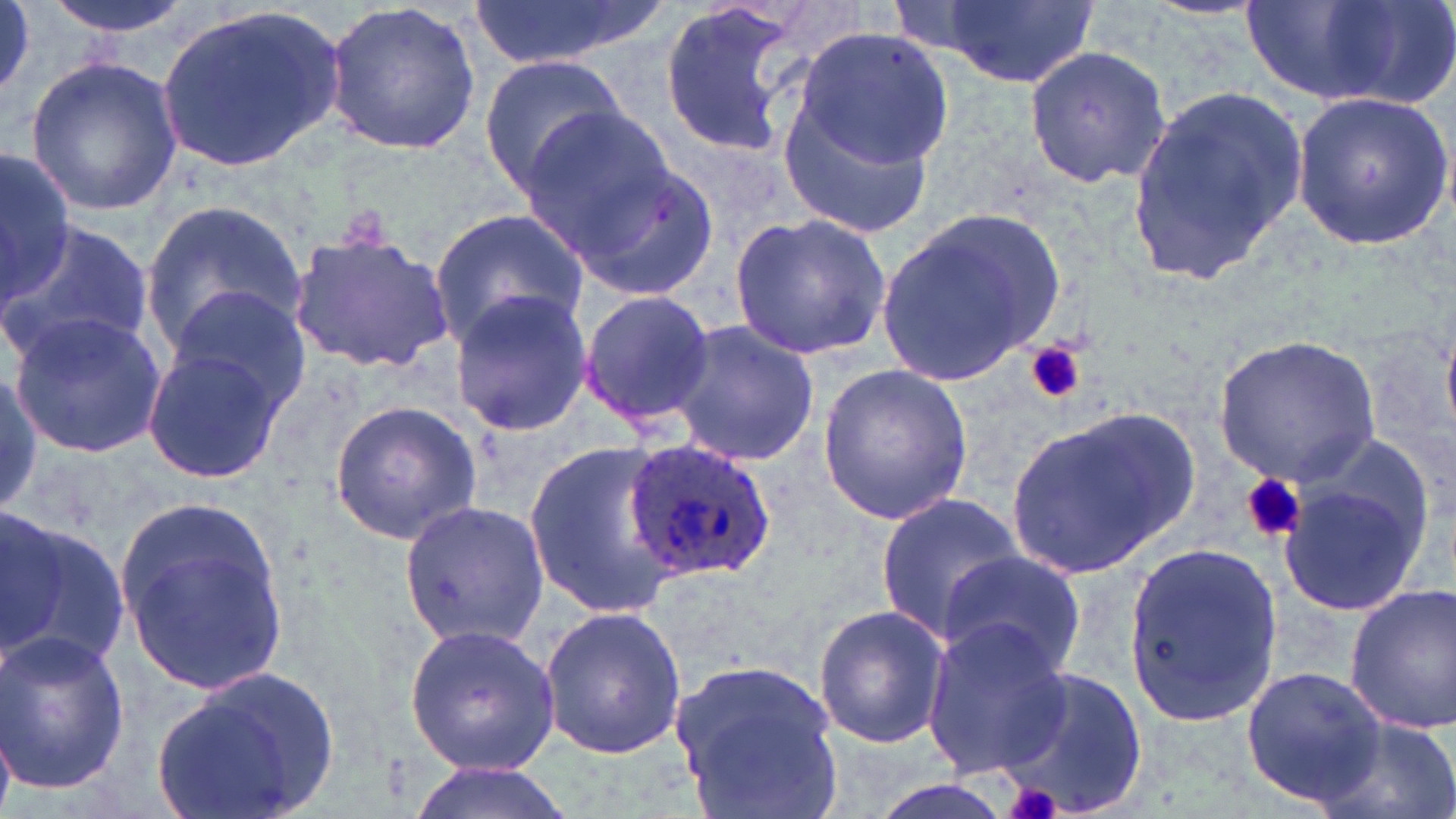

{
  "slide_level_diagnosis": "Plasmodium ovale",
  "modality": "optical microscopy",
  "uninfected_red_blood_cell_locations": "approximate bounding boxes as (x1,y1)-(x2,y2) corner pairs in pixels: (44,0)-(195,42), (472,0)-(669,69), (655,0)-(804,157), (915,0)-(1102,89), (0,1)-(34,96), (325,1)-(483,155), (1235,3)-(1435,110), (152,4)-(347,174), (792,25)-(954,173), (1024,44)-(1172,190), (24,56)-(184,216), (479,57)-(631,200), (1127,83)-(1310,283), (780,86)-(939,240), (1290,93)-(1455,248), (518,105)-(678,261), (0,146)-(75,303), (559,152)-(719,302), (141,198)-(307,354), (876,204)-(1068,388), (429,206)-(590,349), (729,213)-(891,361), (0,219)-(154,367), (288,226)-(454,373), (163,283)-(311,419), (445,286)-(590,437), (577,288)-(716,433), (7,313)-(166,457), (667,318)-(819,468), (1213,334)-(1383,484), (140,347)-(284,487), (816,363)-(976,526), (0,371)-(43,513), (328,400)-(482,544), (1006,402)-(1202,578), (522,438)-(684,619), (1274,458)-(1430,622), (874,490)-(1025,641), (397,499)-(549,651), (115,501)-(290,697), (6,511)-(133,679), (1122,541)-(1282,730), (941,549)-(1086,681), (1342,583)-(1456,734), (540,605)-(688,760), (813,605)-(951,748), (921,619)-(1072,776), (402,622)-(562,778), (0,628)-(132,798), (667,655)-(846,819), (148,664)-(343,819), (1241,664)-(1391,808), (991,667)-(1150,819), (1313,714)-(1456,819), (401,760)-(581,819), (865,777)-(1019,819)",
  "stain": "May-Grünwald-Giemsa",
  "field_of_view": "one of a larger specimen",
  "platelet_locations": "approximate bounding boxes as (x1,y1)-(x2,y2) corner pairs in pixels: (1026,341)-(1086,404), (1242,474)-(1307,545), (997,782)-(1068,819)",
  "magnification": "1000x",
  "preparation": "thin blood film",
  "image_size": "1456×819 pixels",
  "plasmodium_ovale_infected_red_blood_cell_locations": "approximate bounding boxes as (x1,y1)-(x2,y2) corner pairs in pixels: (622,436)-(778,579)"
}